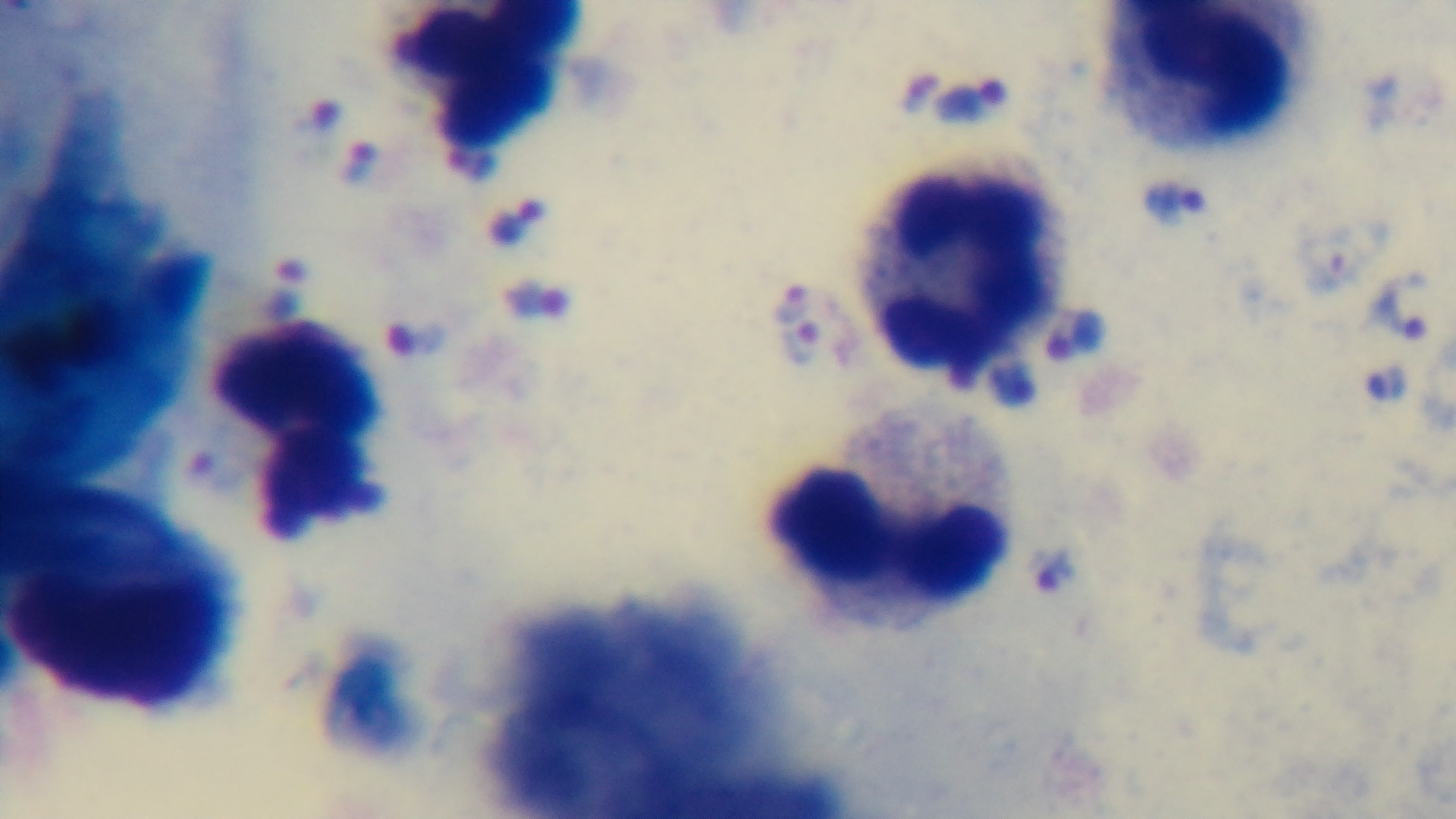

Giemsa stain. Oil-immersion objective, 100x. One field from the slide. Malaria status: positive. Preparation: thick smear. Captured with a mounted 4K digital camera. Photomicrograph.